Identify the parasite.
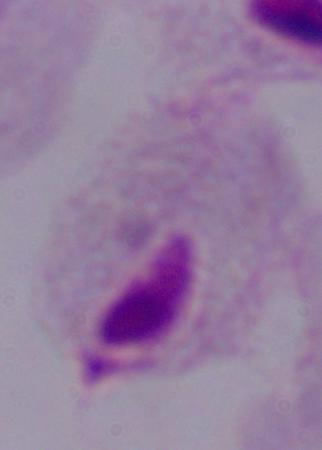
A trichomonad.

Summary:
  - Magnification: 1000x
  - Modality: photomicrograph